Classify this cell by malaria status.
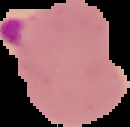

Parasitized.

Image is 130×127 pixels. From a thin blood smear. Segmented cell region on a black background.